Point out each leukocyte.
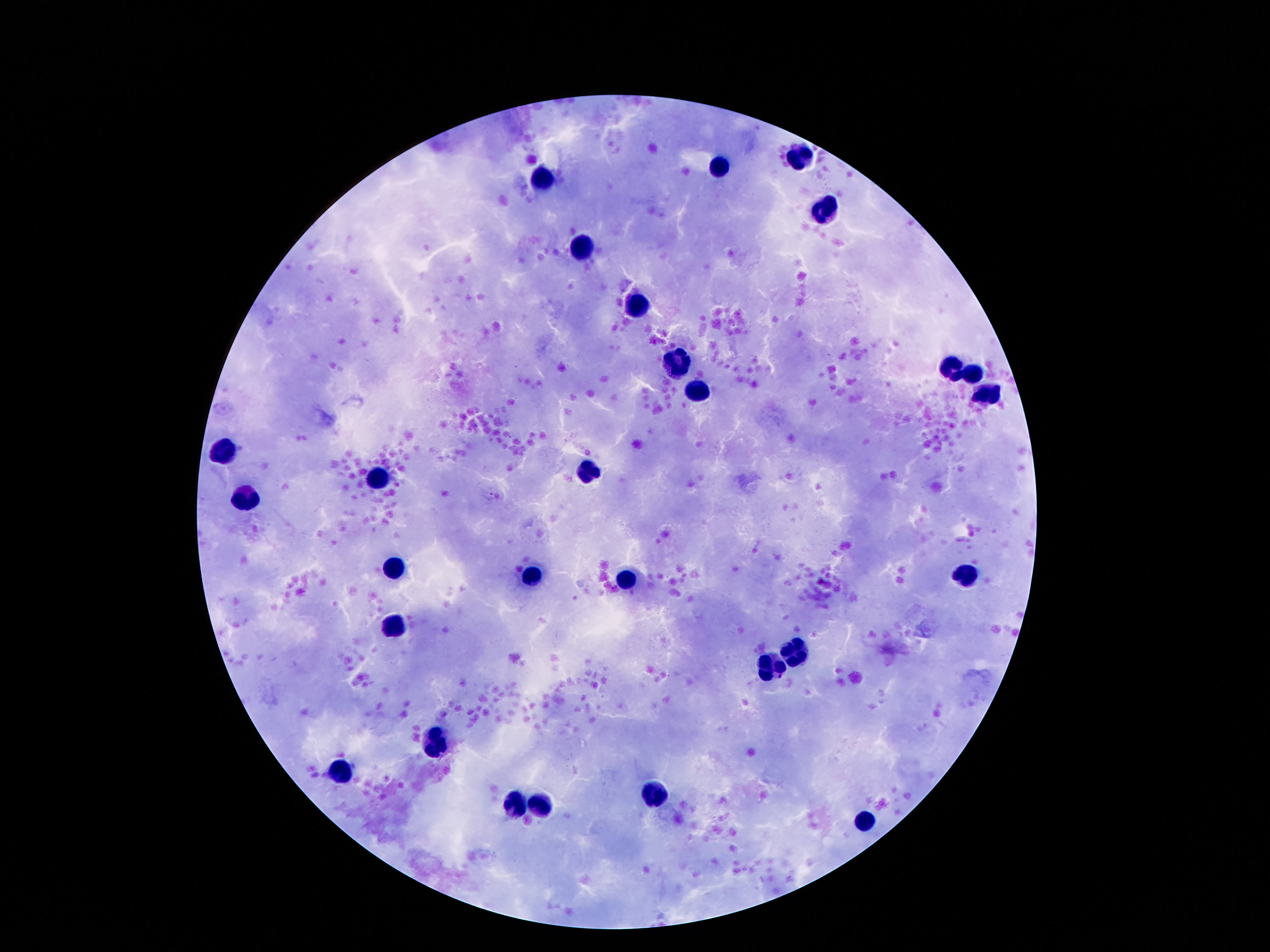
Approximate centers as {x, y} in pixels.
Leukocytes: {799, 157}, {715, 168}, {542, 180}, {824, 210}, {582, 246}, {631, 304}, {675, 361}, {957, 368}, {972, 373}, {698, 390}, {989, 390}, {226, 451}, {591, 469}, {379, 477}, {248, 499}, {396, 567}, {965, 575}, {532, 578}, {626, 580}, {396, 622}, {794, 651}, {769, 664}, {433, 741}, {339, 770}, {656, 793}, {517, 803}, {544, 803}, {866, 822}.

Photographed through the microscope eyepiece with a smartphone camera. Single field of view. Image is 1270×952 pixels. 100x magnification. Giemsa stain. Thick blood smear. Patient malaria status: uninfected.